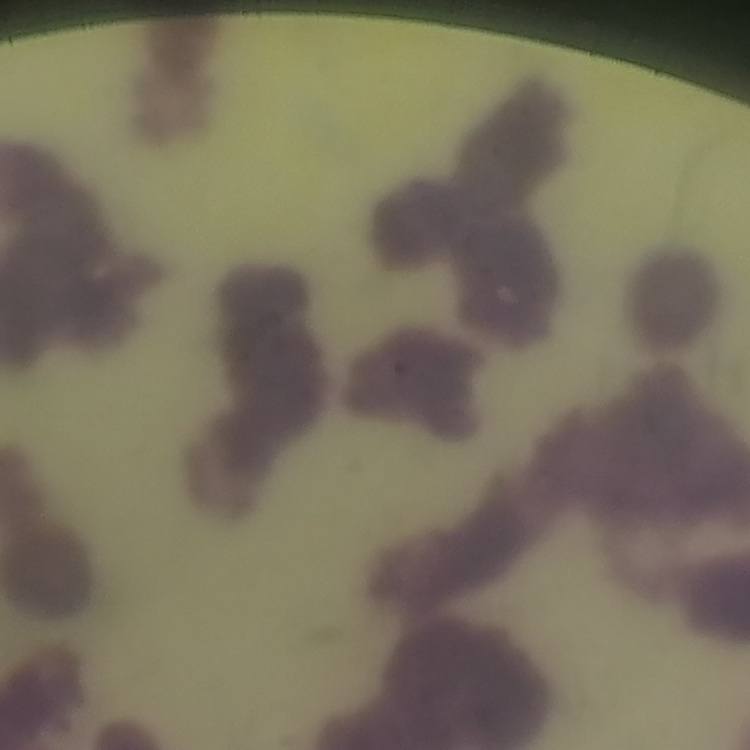

Summary:
  - Erythrocyte morphology: rouleaux formation
  - Image type: one tile cut from a larger photomicrograph
  - Preparation: thin peripheral smear
  - Stain: Field's or Giemsa